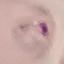

Malaria status: parasitized. Photographed with a smartphone camera at the microscope eyepiece. Giemsa-stained preparation. Automatically extracted cell patch, resized to 64 × 64 pixels. Thin blood smear.